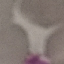

Summary:
  - Malaria status: uninfected
  - Preparation: thin blood smear
  - Stain: Giemsa
  - Capture: smartphone through the microscope eyepiece
  - Image type: automatically extracted cell patch, resized to 64 × 64 pixels